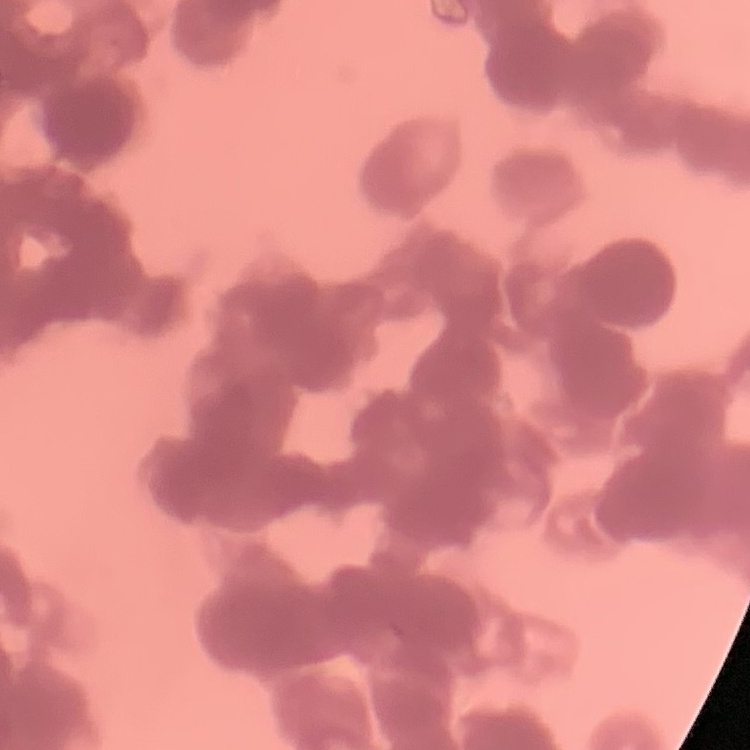

{
  "erythrocyte_morphology": "rouleaux formation",
  "stain": "Field's or Giemsa",
  "preparation": "thin blood film",
  "image_type": "one tile cut from a larger photomicrograph"
}